State which parasite is depicted.
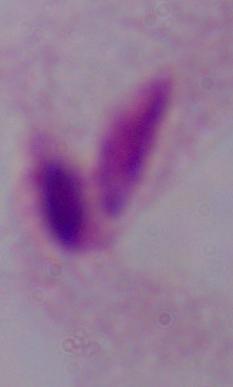
A trichomonad.

Summary:
  - Modality: micrograph
  - Magnification: 1000x